Name the cell type shown.
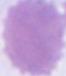

This is an erythrocyte.

modality = photomicrograph
magnification = 1000x